Name the cell type shown.
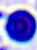

A leukocyte.

Photomicrograph. Captured at 400x magnification.